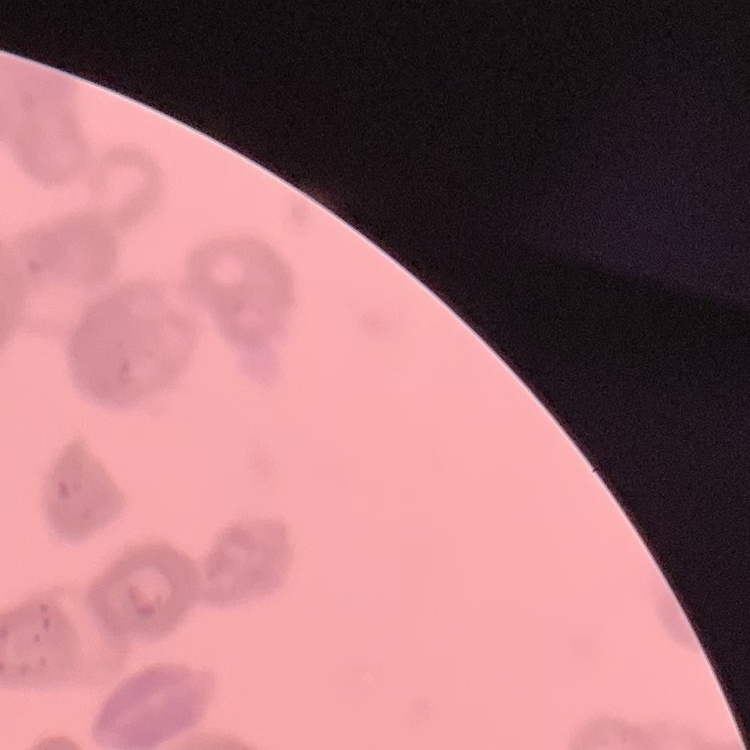
{
  "red_blood_cell_morphology": "rouleaux formation",
  "image_type": "square crop of a larger photomicrograph",
  "preparation": "thin blood film",
  "stain": "Field's or Giemsa"
}